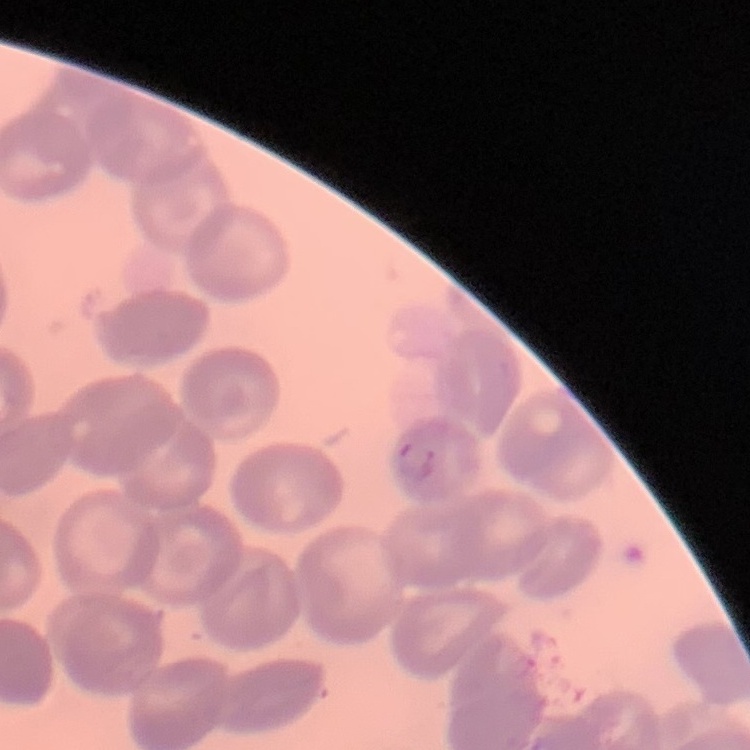

{
  "erythrocyte_morphology": "no rouleaux formation",
  "stain": "Field's or Giemsa",
  "preparation": "thin blood smear",
  "image_type": "square crop of a larger photomicrograph"
}